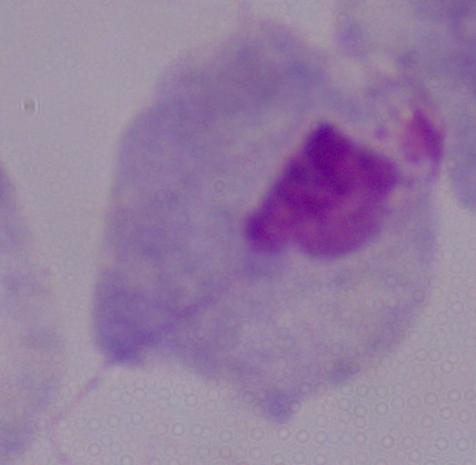

identification = trichomonad
magnification = 1000x
modality = micrograph